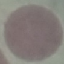

Malaria status: uninfected. Thin blood film. Cell patch, automatically extracted from a larger field of view and resized to 64 × 64 pixels. Acquired by smartphone through the microscope eyepiece. Giemsa-stained preparation.